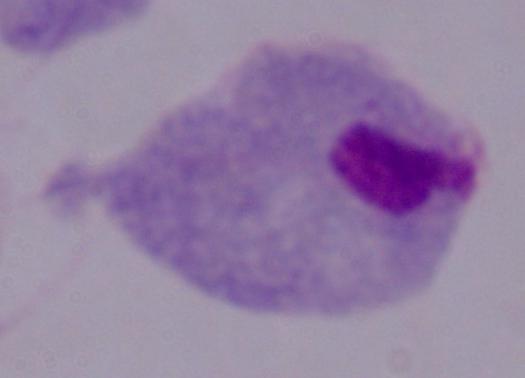

1000x magnification. Photomicrograph. A trichomonad is seen.